Classify this cell by malaria status.
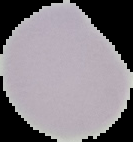

Uninfected.

Summary:
  - Image type: cell region segmented out of the field of view; surrounding area masked to black
  - Preparation: thin blood film
  - Image size: 133×142 pixels